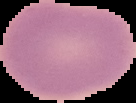
Summary:
  - Preparation: thin blood film
  - Image type: segmented cell region with the area outside set to black
  - Result: no Plasmodium parasites seen
  - Image size: 136×103 pixels